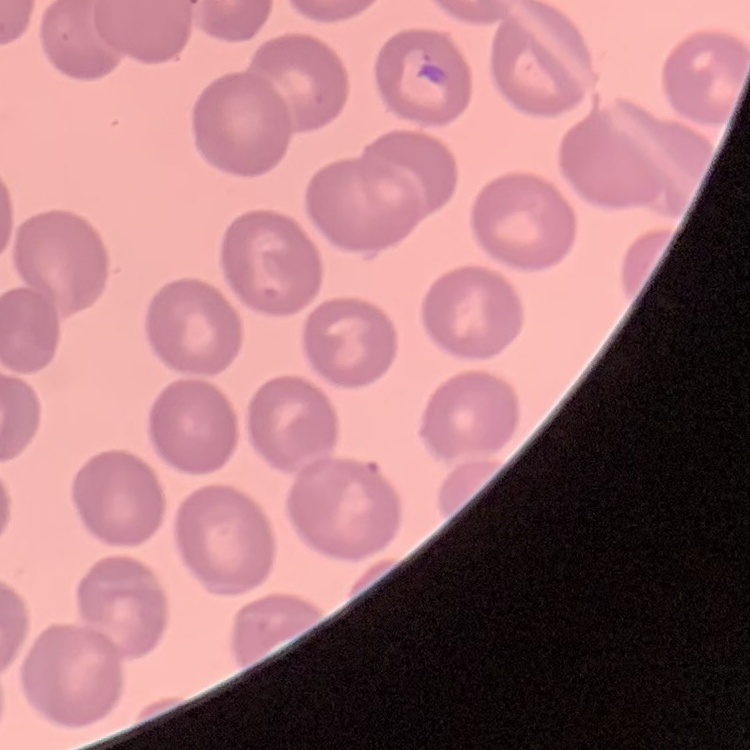
Summary:
  - Red blood cell morphology: no rouleaux formation
  - Stain: Field's or Giemsa
  - Preparation: thin peripheral smear
  - Image type: one tile cut from a larger photomicrograph